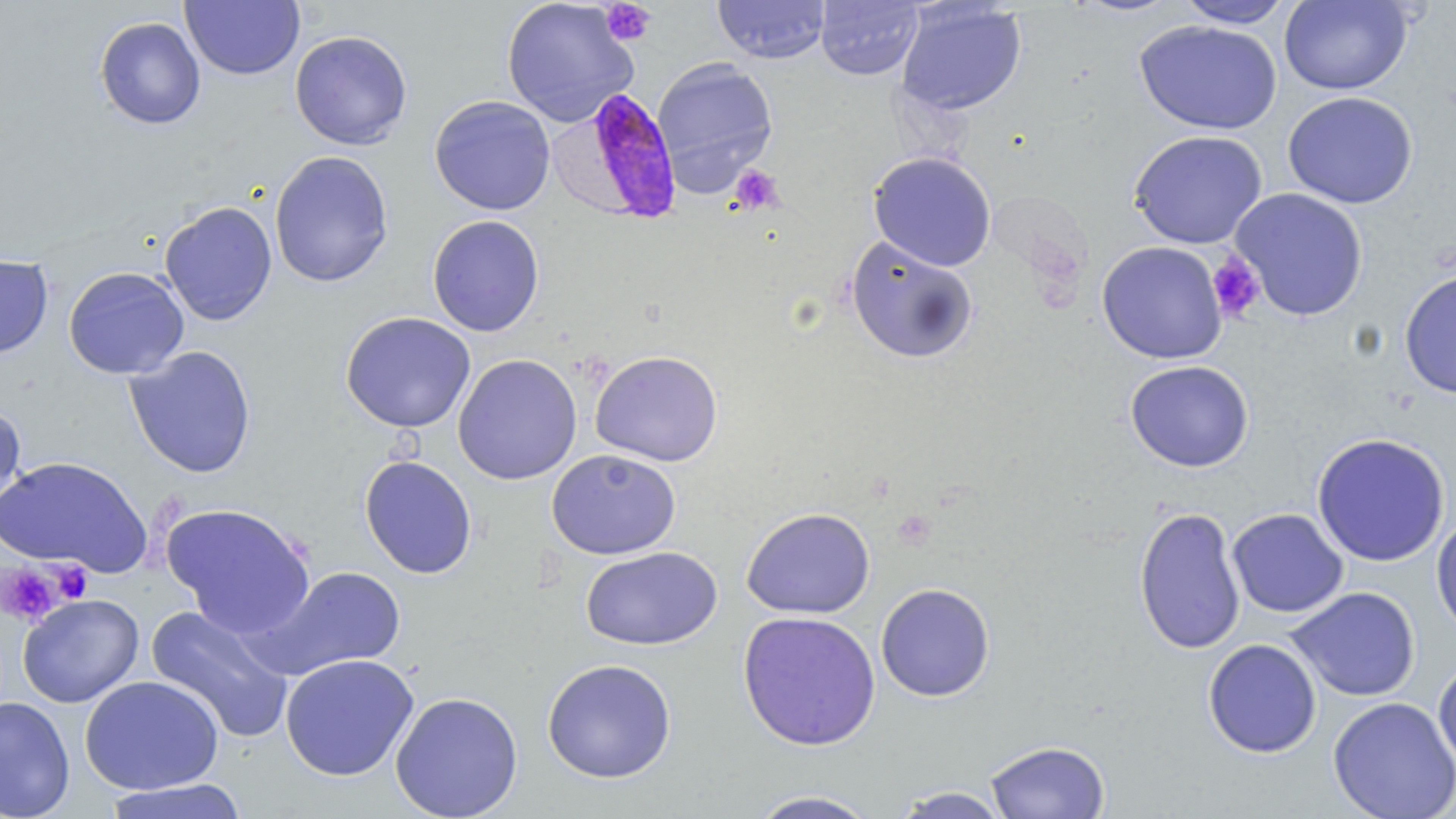
slide-level diagnosis = Plasmodium falciparum
field of view = single
magnification = 1000x
platelet locations = approximate bounding boxes as [x1, y1, x2, y2] in pixels: [600, 1, 656, 47], [729, 165, 784, 215], [1207, 252, 1266, 322], [1, 562, 66, 626], [48, 562, 94, 604]
preparation = thin blood film
image size = 1456×819 pixels
uninfected red blood cell locations = approximate bounding boxes as [x1, y1, x2, y2] in pixels: [500, 0, 639, 128], [712, 0, 830, 63], [815, 0, 924, 81], [1068, 0, 1183, 17], [1175, 0, 1296, 28], [180, 1, 305, 81], [1278, 1, 1414, 95], [895, 2, 1027, 116], [94, 16, 206, 130], [1134, 19, 1282, 135], [289, 30, 412, 150], [652, 57, 778, 186], [1283, 90, 1418, 209], [429, 95, 556, 215], [1128, 130, 1268, 249], [269, 150, 394, 288], [868, 151, 997, 271], [1229, 188, 1368, 321], [159, 200, 278, 326], [428, 214, 545, 337], [845, 236, 979, 364], [1097, 241, 1228, 364], [0, 253, 53, 359], [64, 266, 189, 379], [1399, 269, 1456, 399], [340, 312, 476, 433], [124, 345, 257, 479], [590, 349, 724, 467], [452, 353, 582, 485], [1125, 359, 1254, 472], [0, 402, 27, 525], [1312, 432, 1450, 566], [546, 449, 681, 560], [0, 455, 152, 576], [359, 455, 478, 579], [161, 502, 316, 637], [1133, 505, 1246, 655], [741, 506, 875, 619], [1227, 508, 1348, 618], [1431, 511, 1456, 642], [580, 546, 722, 650], [257, 565, 406, 679], [876, 583, 995, 702], [1285, 586, 1421, 702], [17, 593, 144, 708], [145, 603, 294, 744], [737, 610, 881, 751], [1203, 638, 1322, 758], [280, 653, 419, 782], [1433, 656, 1456, 775], [541, 658, 677, 784], [80, 675, 224, 795], [390, 691, 524, 819], [0, 696, 75, 819], [1328, 696, 1456, 819], [984, 740, 1110, 819], [103, 778, 251, 819], [888, 786, 1014, 818], [747, 789, 882, 818]
Plasmodium falciparum-infected red blood cell locations = approximate bounding boxes as [x1, y1, x2, y2] in pixels: [576, 86, 685, 224]
modality = optical microscopy
stain = May-Grünwald-Giemsa